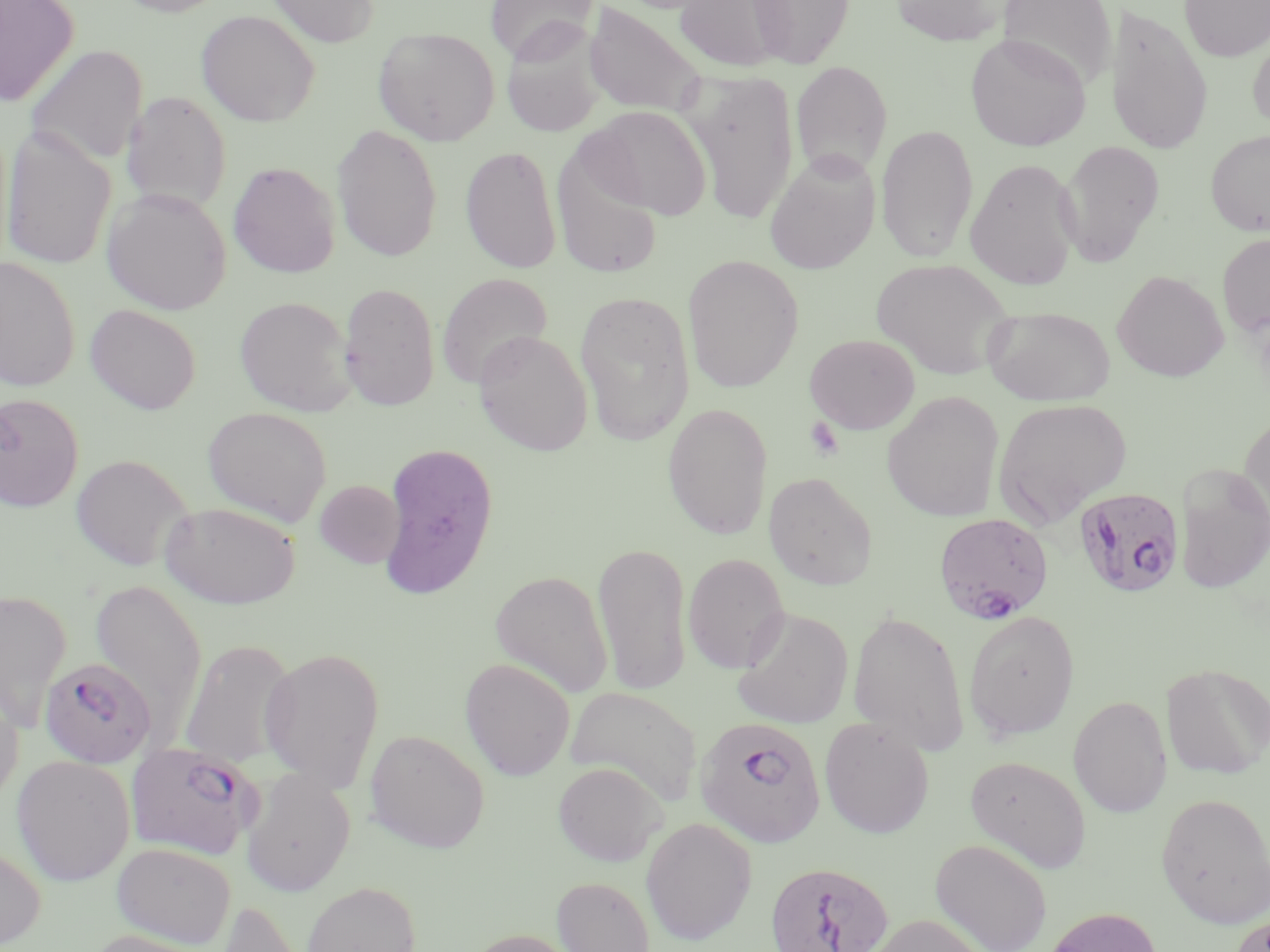
Summary:
  - Coordinate format: approximate bounding boxes as named x1/y1/x2/y2 corners in pixels
  - Uninfected red blood cell locations: (x1=0, y1=0, x2=79, y2=106), (x1=111, y1=0, x2=233, y2=17), (x1=263, y1=0, x2=380, y2=48), (x1=485, y1=0, x2=599, y2=63), (x1=674, y1=0, x2=791, y2=73), (x1=749, y1=0, x2=855, y2=69), (x1=889, y1=0, x2=1010, y2=47), (x1=997, y1=0, x2=1117, y2=89), (x1=1179, y1=0, x2=1270, y2=61), (x1=583, y1=2, x2=708, y2=117), (x1=1105, y1=5, x2=1214, y2=156), (x1=196, y1=9, x2=319, y2=127), (x1=500, y1=23, x2=607, y2=138), (x1=373, y1=27, x2=500, y2=145), (x1=1247, y1=30, x2=1270, y2=133), (x1=965, y1=33, x2=1091, y2=151), (x1=25, y1=44, x2=148, y2=167), (x1=791, y1=62, x2=893, y2=180), (x1=687, y1=71, x2=798, y2=225), (x1=121, y1=91, x2=231, y2=213), (x1=582, y1=105, x2=712, y2=220), (x1=876, y1=123, x2=978, y2=264), (x1=331, y1=124, x2=442, y2=263), (x1=1, y1=125, x2=116, y2=271), (x1=1205, y1=130, x2=1270, y2=236), (x1=1057, y1=139, x2=1166, y2=266), (x1=461, y1=145, x2=562, y2=273), (x1=552, y1=145, x2=664, y2=281), (x1=764, y1=152, x2=880, y2=275), (x1=965, y1=157, x2=1082, y2=290), (x1=228, y1=162, x2=340, y2=278), (x1=101, y1=188, x2=232, y2=315), (x1=1217, y1=232, x2=1270, y2=337), (x1=682, y1=255, x2=804, y2=393), (x1=0, y1=256, x2=81, y2=391), (x1=870, y1=257, x2=1015, y2=379), (x1=1112, y1=269, x2=1228, y2=382), (x1=436, y1=273, x2=553, y2=388), (x1=338, y1=281, x2=441, y2=411), (x1=575, y1=291, x2=695, y2=446), (x1=234, y1=295, x2=358, y2=416), (x1=85, y1=304, x2=201, y2=414), (x1=982, y1=305, x2=1116, y2=406), (x1=474, y1=330, x2=593, y2=456), (x1=804, y1=333, x2=920, y2=434), (x1=882, y1=391, x2=1005, y2=522), (x1=0, y1=393, x2=84, y2=513), (x1=992, y1=397, x2=1132, y2=527), (x1=662, y1=402, x2=774, y2=539), (x1=202, y1=406, x2=332, y2=527), (x1=1237, y1=410, x2=1270, y2=544), (x1=378, y1=441, x2=499, y2=599), (x1=70, y1=454, x2=193, y2=571), (x1=1175, y1=464, x2=1270, y2=594), (x1=763, y1=472, x2=879, y2=590), (x1=315, y1=480, x2=405, y2=568), (x1=160, y1=501, x2=301, y2=608), (x1=593, y1=540, x2=693, y2=696), (x1=683, y1=552, x2=790, y2=673), (x1=490, y1=569, x2=614, y2=698), (x1=89, y1=577, x2=208, y2=741), (x1=0, y1=589, x2=72, y2=728), (x1=733, y1=606, x2=854, y2=730), (x1=848, y1=608, x2=970, y2=756), (x1=963, y1=609, x2=1080, y2=742), (x1=178, y1=637, x2=297, y2=768), (x1=260, y1=647, x2=385, y2=792), (x1=460, y1=658, x2=576, y2=780), (x1=1161, y1=663, x2=1270, y2=780), (x1=0, y1=684, x2=24, y2=808), (x1=563, y1=685, x2=703, y2=807), (x1=1069, y1=695, x2=1171, y2=818), (x1=819, y1=718, x2=935, y2=838), (x1=364, y1=729, x2=489, y2=853), (x1=11, y1=754, x2=135, y2=886), (x1=964, y1=754, x2=1092, y2=874), (x1=553, y1=761, x2=667, y2=866), (x1=242, y1=769, x2=355, y2=897), (x1=1155, y1=791, x2=1270, y2=929), (x1=640, y1=817, x2=758, y2=945), (x1=930, y1=838, x2=1053, y2=952), (x1=112, y1=841, x2=236, y2=948), (x1=0, y1=842, x2=46, y2=950), (x1=552, y1=876, x2=656, y2=952), (x1=301, y1=880, x2=421, y2=952), (x1=215, y1=899, x2=312, y2=952), (x1=1044, y1=906, x2=1163, y2=952), (x1=861, y1=913, x2=992, y2=952), (x1=1227, y1=913, x2=1269, y2=952), (x1=463, y1=928, x2=580, y2=952), (x1=83, y1=929, x2=214, y2=952)
  - Plasmodium falciparum-infected red blood cell locations: (x1=1074, y1=487, x2=1185, y2=598), (x1=933, y1=512, x2=1054, y2=625), (x1=39, y1=657, x2=157, y2=768), (x1=695, y1=716, x2=827, y2=848), (x1=126, y1=741, x2=260, y2=860), (x1=764, y1=860, x2=893, y2=952)
  - Platelet locations: (x1=805, y1=417, x2=845, y2=461)
  - Slide-level diagnosis: Plasmodium falciparum
  - Stain: May-Grünwald-Giemsa
  - Preparation: thin blood film
  - Modality: optical microscopy
  - Image size: 1270×952 pixels
  - Magnification: 1000x
  - Field of view: one of a larger specimen